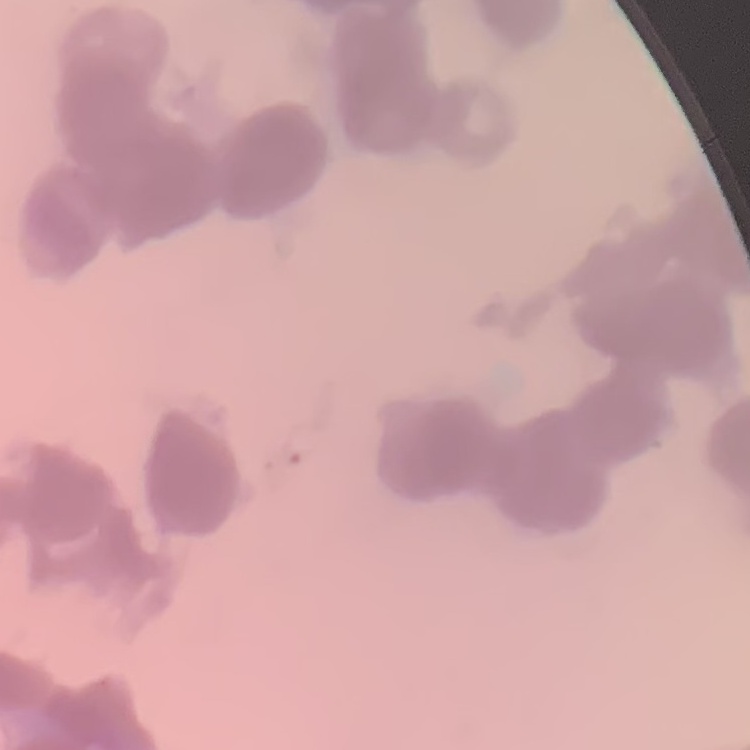

{
  "red_blood_cell_morphology": "rouleaux formation",
  "image_type": "one tile cut from a larger photomicrograph",
  "stain": "Field's or Giemsa",
  "preparation": "thin peripheral smear"
}